Identify the cell.
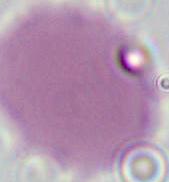
This is an erythrocyte.

{
  "modality": "photomicrograph",
  "magnification": "1000x"
}